Outline each Plasmodium ovale-infected red blood cell.
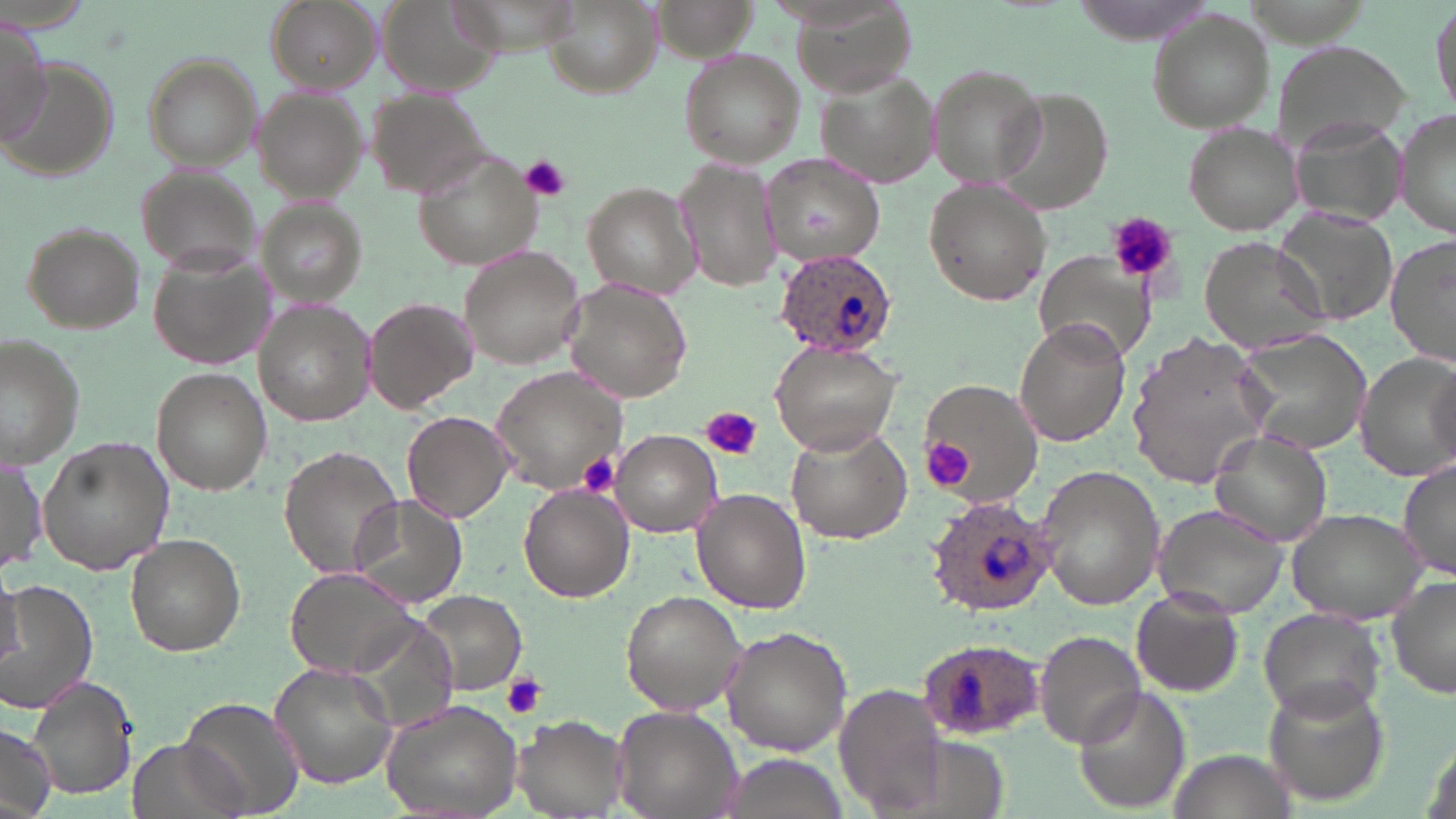
Approximate bounding boxes as named x1/y1/x2/y2 corners in pixels.
Plasmodium ovale-infected red blood cells: (x1=771, y1=251, x2=897, y2=359), (x1=924, y1=493, x2=1055, y2=617), (x1=915, y1=636, x2=1045, y2=739).

Summary:
  - Platelet locations: (x1=520, y1=154, x2=571, y2=201), (x1=1107, y1=212, x2=1177, y2=282), (x1=701, y1=406, x2=762, y2=462), (x1=920, y1=437, x2=978, y2=492), (x1=581, y1=453, x2=621, y2=494), (x1=500, y1=674, x2=544, y2=719)
  - Uninfected red blood cell locations: (x1=264, y1=0, x2=380, y2=87), (x1=648, y1=0, x2=757, y2=67), (x1=540, y1=1, x2=658, y2=96), (x1=796, y1=1, x2=915, y2=100), (x1=1428, y1=3, x2=1454, y2=119), (x1=373, y1=4, x2=505, y2=98), (x1=1145, y1=12, x2=1276, y2=132), (x1=0, y1=16, x2=52, y2=143), (x1=1272, y1=41, x2=1411, y2=153), (x1=678, y1=47, x2=806, y2=169), (x1=138, y1=53, x2=261, y2=169), (x1=0, y1=60, x2=119, y2=184), (x1=926, y1=62, x2=1045, y2=186), (x1=818, y1=66, x2=940, y2=187), (x1=251, y1=88, x2=368, y2=200), (x1=996, y1=88, x2=1112, y2=214), (x1=363, y1=90, x2=493, y2=200), (x1=1396, y1=102, x2=1455, y2=242), (x1=1182, y1=122, x2=1302, y2=235), (x1=413, y1=152, x2=550, y2=272), (x1=760, y1=155, x2=890, y2=271), (x1=676, y1=157, x2=781, y2=294), (x1=133, y1=167, x2=260, y2=273), (x1=924, y1=179, x2=1052, y2=306), (x1=583, y1=181, x2=707, y2=302), (x1=259, y1=196, x2=367, y2=304), (x1=1273, y1=213, x2=1403, y2=329), (x1=20, y1=222, x2=147, y2=333), (x1=1386, y1=232, x2=1456, y2=364), (x1=1198, y1=236, x2=1331, y2=353), (x1=458, y1=244, x2=587, y2=368), (x1=148, y1=251, x2=270, y2=372), (x1=1034, y1=253, x2=1160, y2=366), (x1=563, y1=278, x2=694, y2=403), (x1=365, y1=298, x2=475, y2=415), (x1=256, y1=301, x2=370, y2=426), (x1=1015, y1=317, x2=1129, y2=446), (x1=1234, y1=330, x2=1369, y2=456), (x1=1129, y1=333, x2=1272, y2=486), (x1=1, y1=335, x2=85, y2=469), (x1=770, y1=340, x2=901, y2=456), (x1=1356, y1=354, x2=1456, y2=482), (x1=490, y1=367, x2=630, y2=496), (x1=151, y1=368, x2=269, y2=496), (x1=920, y1=377, x2=1042, y2=506), (x1=401, y1=411, x2=514, y2=524), (x1=785, y1=423, x2=911, y2=544), (x1=608, y1=429, x2=722, y2=536), (x1=1208, y1=429, x2=1333, y2=545), (x1=37, y1=436, x2=174, y2=576), (x1=277, y1=445, x2=404, y2=580), (x1=1, y1=453, x2=46, y2=574), (x1=1397, y1=458, x2=1456, y2=579), (x1=1034, y1=465, x2=1166, y2=611), (x1=518, y1=484, x2=633, y2=600), (x1=693, y1=489, x2=811, y2=613), (x1=349, y1=495, x2=467, y2=610), (x1=1153, y1=502, x2=1292, y2=618), (x1=1286, y1=506, x2=1428, y2=622), (x1=125, y1=534, x2=245, y2=656), (x1=284, y1=566, x2=424, y2=678), (x1=0, y1=573, x2=25, y2=671), (x1=1386, y1=577, x2=1456, y2=702), (x1=5, y1=579, x2=99, y2=713), (x1=1131, y1=586, x2=1244, y2=696), (x1=415, y1=590, x2=526, y2=696), (x1=620, y1=590, x2=746, y2=716), (x1=1257, y1=607, x2=1385, y2=723), (x1=722, y1=626, x2=851, y2=755), (x1=1032, y1=629, x2=1148, y2=750), (x1=270, y1=663, x2=399, y2=790), (x1=21, y1=674, x2=138, y2=802), (x1=1261, y1=678, x2=1390, y2=809), (x1=834, y1=685, x2=950, y2=811), (x1=1075, y1=686, x2=1190, y2=812), (x1=178, y1=693, x2=306, y2=817), (x1=379, y1=698, x2=524, y2=819), (x1=612, y1=704, x2=743, y2=818), (x1=513, y1=714, x2=627, y2=817), (x1=0, y1=722, x2=56, y2=817), (x1=126, y1=737, x2=246, y2=819), (x1=1171, y1=747, x2=1292, y2=818), (x1=724, y1=753, x2=845, y2=819)
  - Slide-level diagnosis: Plasmodium ovale
  - Field of view: one of a larger specimen
  - Magnification: 1000x
  - Modality: light microscopy
  - Stain: May-Grünwald-Giemsa
  - Image size: 1456×819 pixels
  - Preparation: thin blood film